Report the malaria status of this cell.
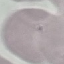

Uninfected.

Summary:
  - Capture: smartphone through the microscope eyepiece
  - Preparation: thin blood smear
  - Stain: Giemsa
  - Image type: automatically extracted cell patch, resized to 64 × 64 pixels